Classify this cell by malaria status.
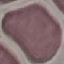
It is uninfected.

Thin smear of blood. Automatically extracted cell patch, resized to 64 × 64 pixels. Photographed with a smartphone camera at the microscope eyepiece. Giemsa stain.